Assess the morphology of the red blood cells.
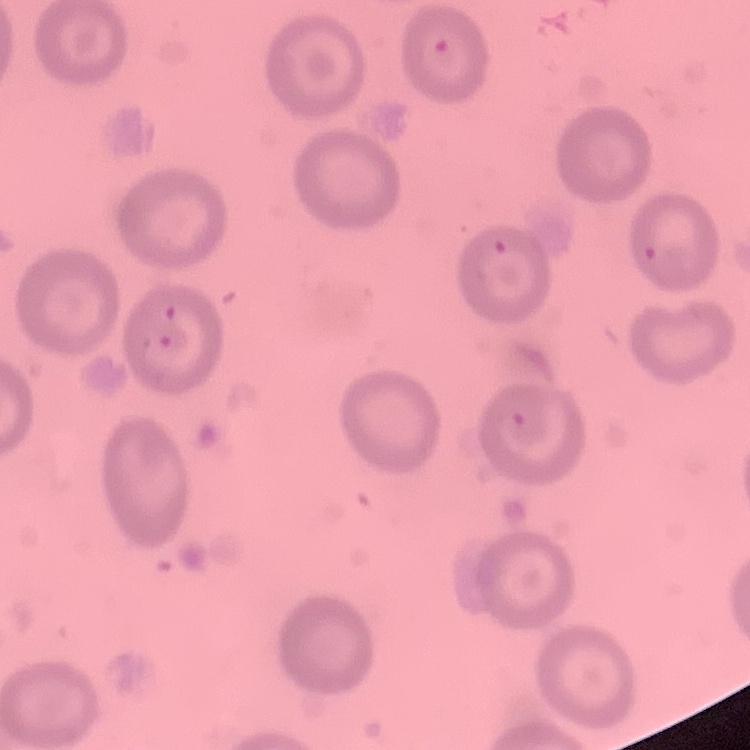
No rouleaux formation.

Thin peripheral smear. Field's or Giemsa stain. Square crop of a larger photomicrograph.